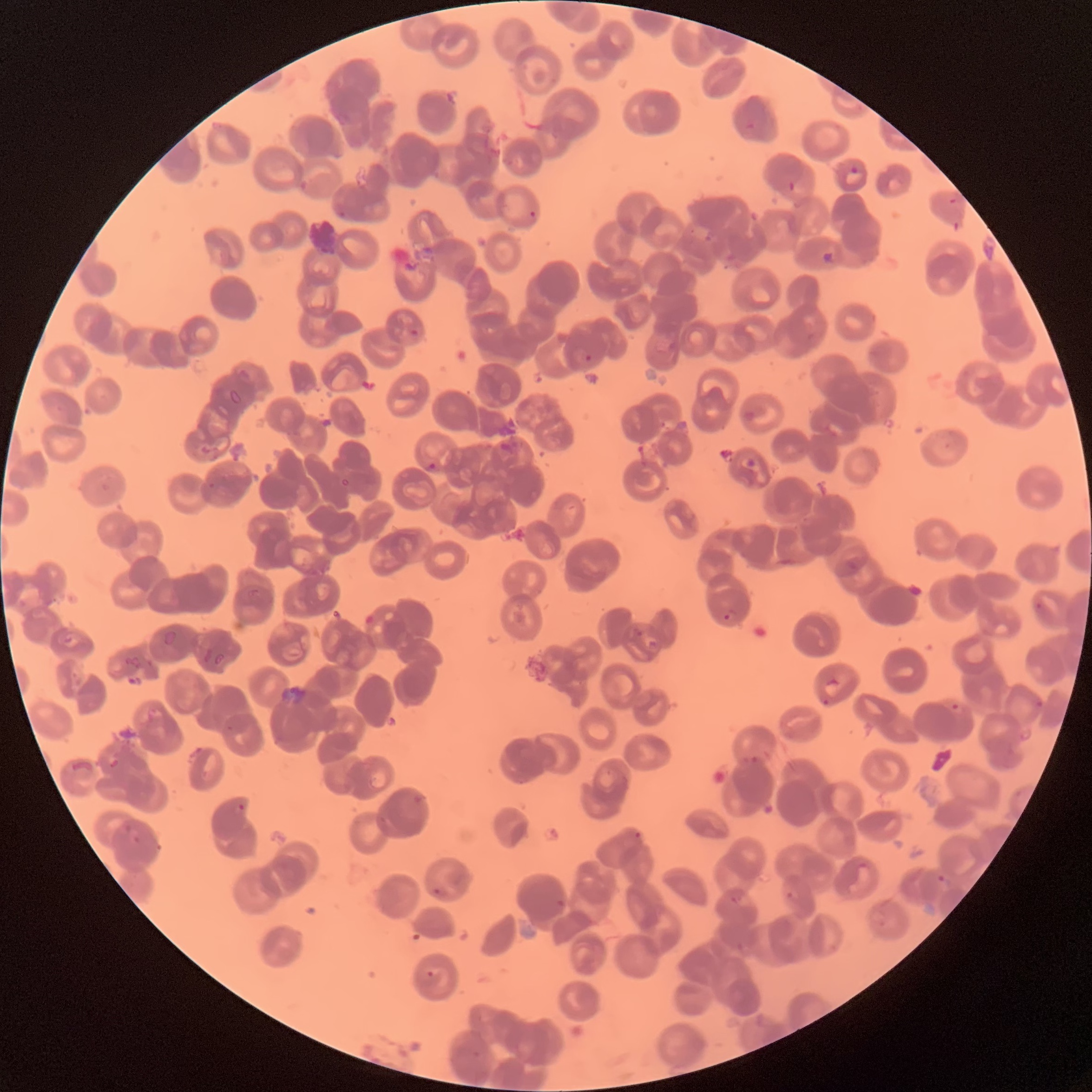
Approximate bounding boxes as (x1, y1, x2, y2) in pixels. Plasmodium parasite locations: (850, 166, 859, 175), (337, 211, 348, 220), (527, 211, 537, 224), (820, 252, 839, 264), (410, 328, 419, 337), (584, 354, 593, 362), (428, 462, 438, 471), (723, 607, 739, 621), (819, 695, 835, 706), (1033, 697, 1044, 708), (946, 700, 963, 711), (235, 802, 245, 811), (126, 825, 143, 843), (857, 860, 871, 870), (937, 873, 952, 890), (432, 887, 446, 897), (786, 890, 798, 900), (730, 895, 752, 906), (555, 899, 566, 908), (427, 971, 435, 977). Plasmodium parasites too small for a box (approximate centers as (x, y) in pixels): (637, 835). Thin blood smear. The red blood cells show rouleaux formation. Optical microscopy. Image is 1092×1092 pixels.